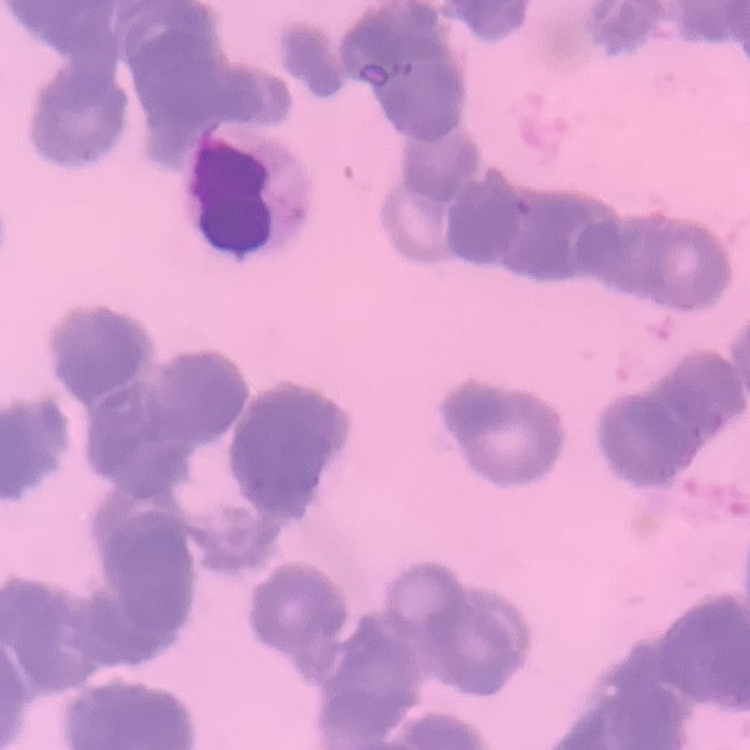

{
  "red_blood_cell_morphology": "rouleaux formation",
  "stain": "Field's or Giemsa",
  "image_type": "one tile cut from a larger photomicrograph",
  "preparation": "thin peripheral smear"
}